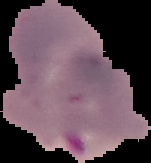

Malaria status: parasitized. From a thin blood smear. Cell region segmented out of the field of view; the surrounding area is masked to black. Image is 151×163 pixels.